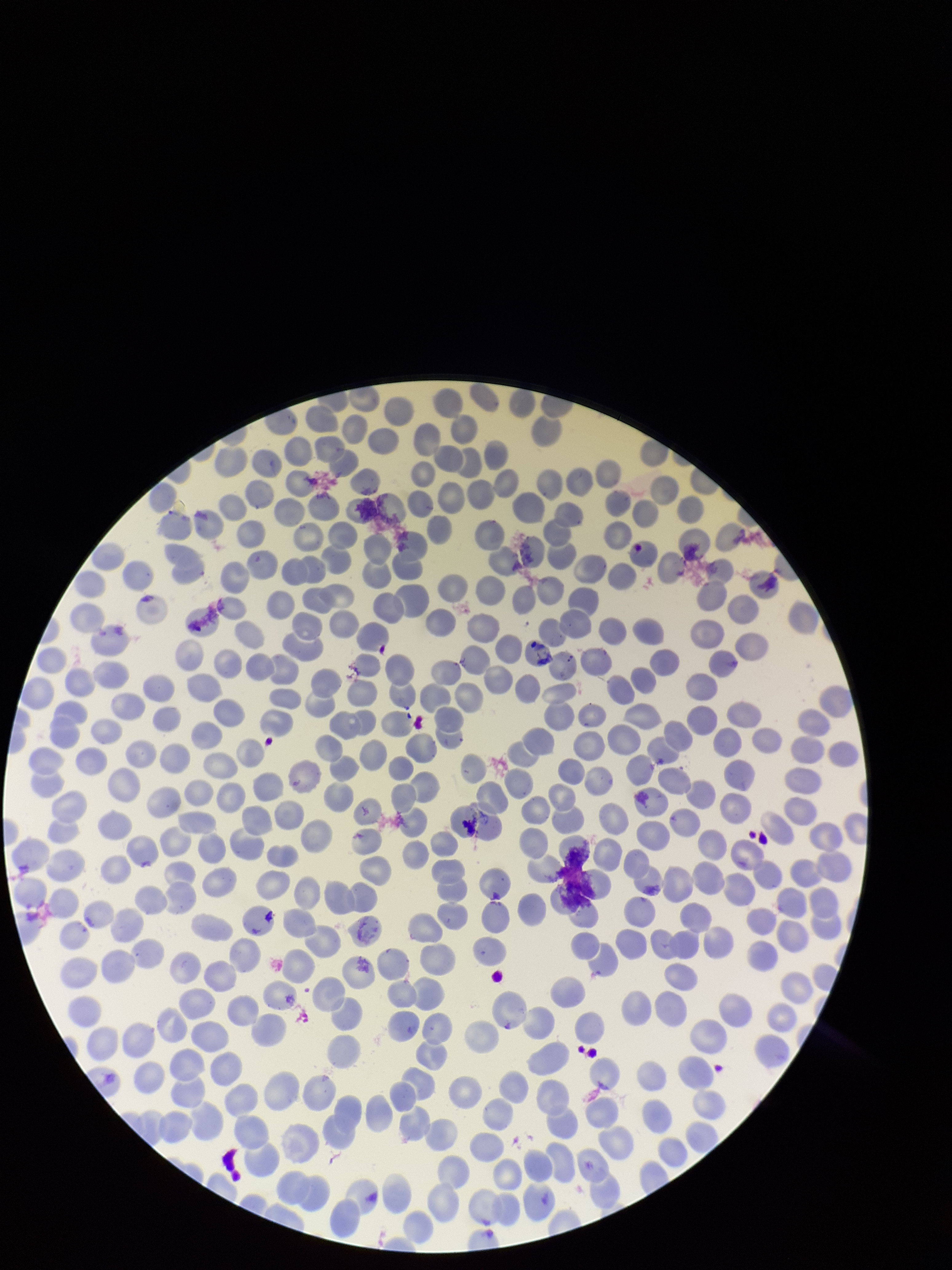

image size = 952×1270 pixels
species reported for this patient = Plasmodium falciparum
preparation = thin blood smear
capture = smartphone photograph through the microscope eyepiece
stain = Giemsa
red blood cell count = 356
parasitized red blood cell count = 0
parasitized red blood cells = none identified
field of view = one from this slide
patient malaria status = positive